Report the malaria status of this cell.
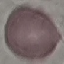
Uninfected.

Acquired by smartphone through the microscope eyepiece. Cell patch, automatically extracted from a larger field of view and resized to 64 × 64 pixels. Giemsa stain. Thin blood film.